Name the parasite shown.
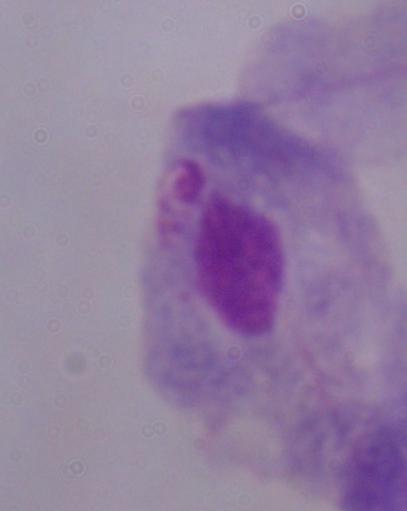

A trichomonad.

modality = micrograph
magnification = 1000x